Identify the parasite.
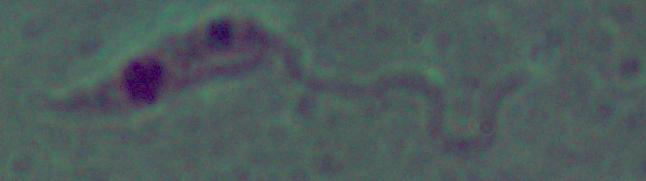
Leishmania.

Photomicrograph. 1000x magnification.